Look for Plasmodium parasites.
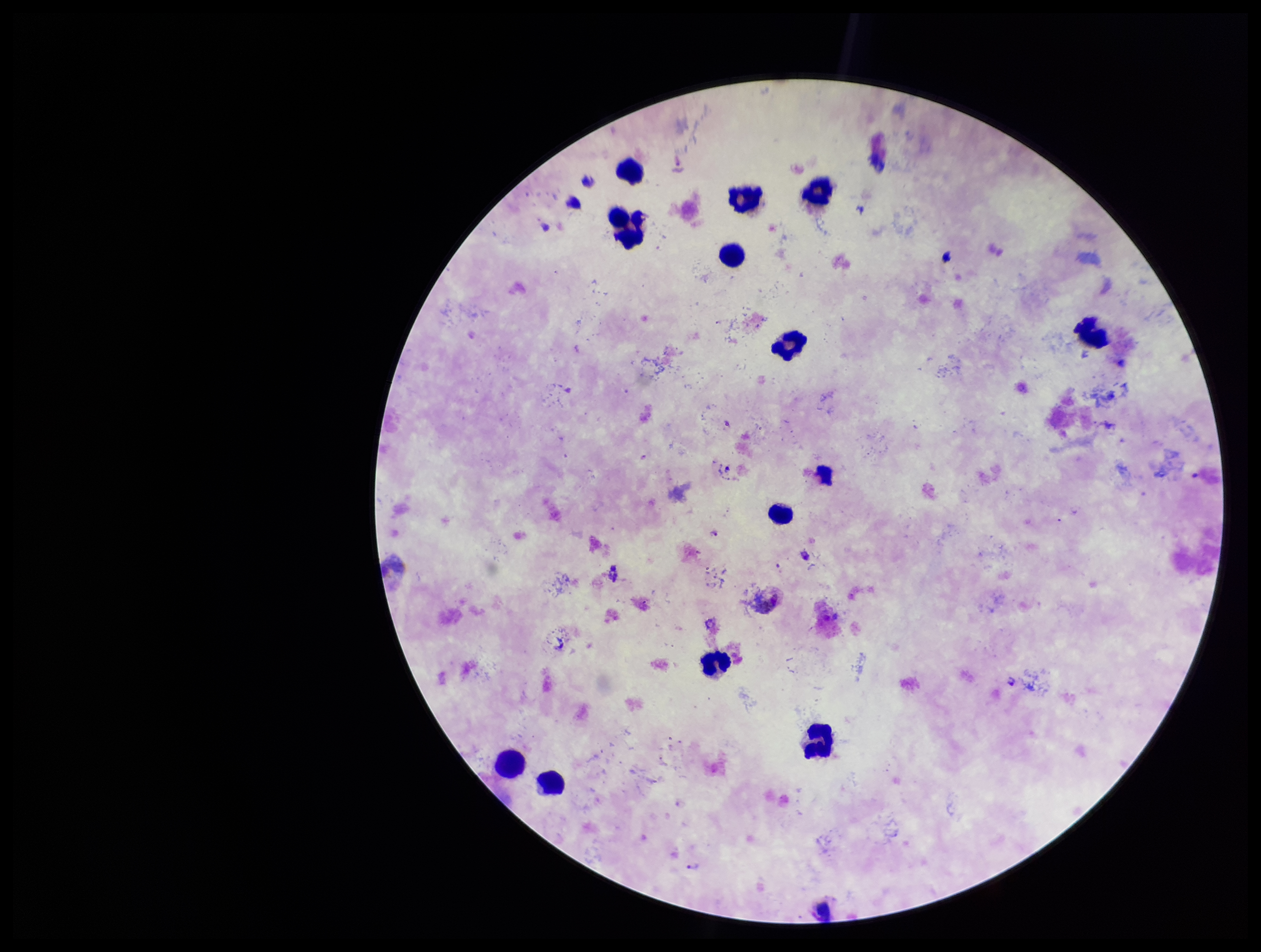
Detected.

{
  "preparation": "thick blood smear",
  "patient_malaria_status": "infected",
  "image_size": "1261×952 pixels",
  "capture": "smartphone photograph through the microscope eyepiece",
  "stain": "Giemsa",
  "parasite_count": 2,
  "species_reported_for_this_patient": "Plasmodium vivax",
  "leukocyte_count": 12,
  "field_of_view": "single"
}